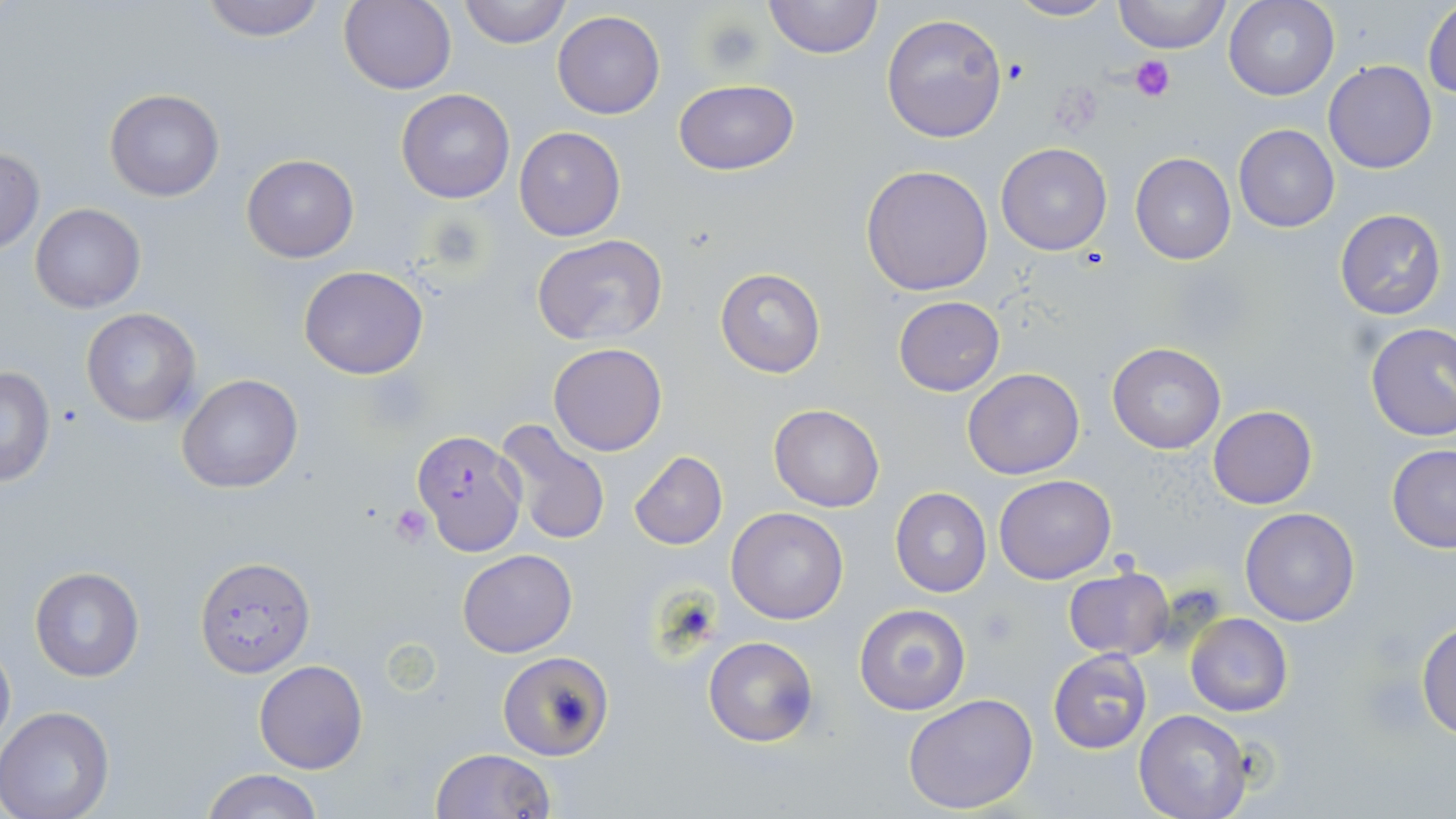
Approximate bounding boxes as [x1, y1, x2, y2] in pixels. Uninfected red blood cell locations: [196, 0, 329, 42], [457, 0, 570, 49], [764, 0, 881, 59], [1006, 0, 1118, 23], [1113, 0, 1232, 54], [1224, 0, 1339, 101], [338, 1, 458, 94], [1423, 3, 1456, 99], [553, 10, 665, 120], [880, 12, 1008, 144], [1324, 59, 1437, 174], [673, 79, 799, 175], [395, 89, 516, 204], [104, 90, 225, 202], [1233, 124, 1340, 232], [513, 127, 625, 241], [995, 142, 1112, 256], [0, 147, 44, 252], [1130, 151, 1236, 266], [240, 154, 359, 263], [861, 164, 993, 295], [31, 203, 145, 312], [1334, 208, 1448, 321], [534, 236, 666, 348], [299, 265, 431, 380], [715, 268, 824, 378], [894, 296, 1004, 397], [80, 308, 201, 428], [1365, 323, 1456, 441], [549, 343, 667, 457], [1108, 343, 1224, 454], [0, 365, 57, 486], [962, 367, 1084, 479], [176, 373, 304, 494], [769, 404, 884, 513], [1208, 405, 1316, 510], [494, 418, 612, 549], [1386, 444, 1456, 553], [629, 450, 727, 549], [994, 475, 1117, 584], [891, 488, 993, 598], [726, 506, 850, 623], [1240, 507, 1361, 627], [457, 549, 577, 658], [193, 554, 314, 679], [29, 566, 143, 681], [1063, 567, 1175, 660], [854, 604, 970, 715], [1185, 613, 1295, 716], [1416, 621, 1456, 736], [0, 634, 14, 754], [702, 637, 818, 748], [1047, 651, 1153, 755], [497, 652, 613, 759], [254, 659, 368, 774], [902, 692, 1039, 815], [0, 707, 117, 819], [1134, 707, 1251, 819], [430, 748, 556, 818], [200, 769, 325, 819]. Platelet locations: [703, 18, 765, 74], [1131, 57, 1175, 101], [390, 505, 435, 546], [976, 604, 1020, 649]. Plasmodium falciparum-infected red blood cell locations: [411, 430, 527, 555]. Slide-level diagnosis: Plasmodium falciparum. Light microscopy. Thin blood film. 1000x magnification. Image is 1456×819 pixels. May-Grünwald-Giemsa-stained preparation. Single field of view.